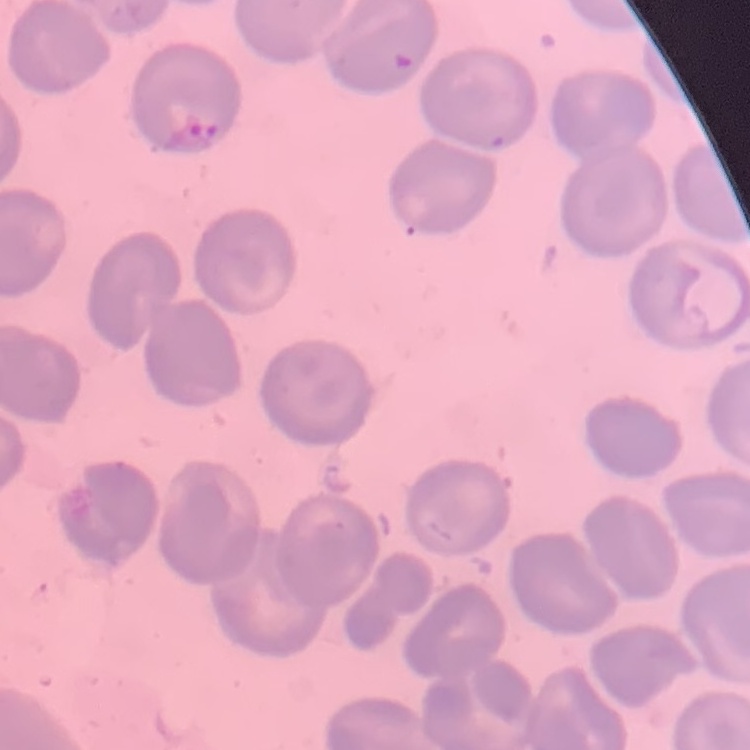

{
  "red_blood_cell_morphology": "no rouleaux formation",
  "stain": "Field's or Giemsa",
  "image_type": "square crop of a larger photomicrograph",
  "preparation": "thin blood smear"
}